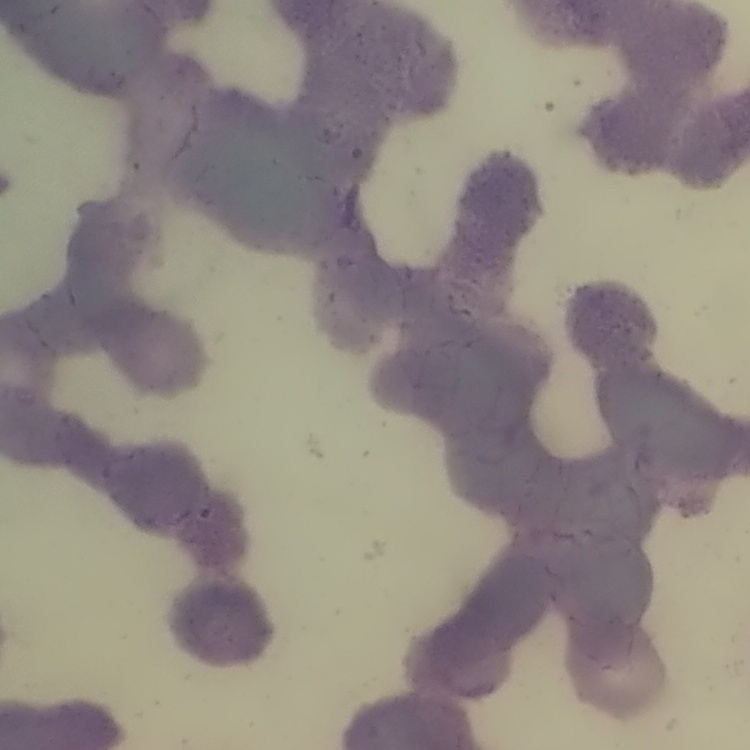

red blood cell morphology = rouleaux formation
preparation = thin blood smear
image type = one tile cut from a larger photomicrograph
stain = Field's or Giemsa